Classify this cell by malaria status.
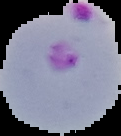
It is parasitized.

{
  "image_size": "121×136 pixels",
  "preparation": "thin blood film",
  "image_type": "cell region segmented out of the field of view; surrounding area masked to black"
}